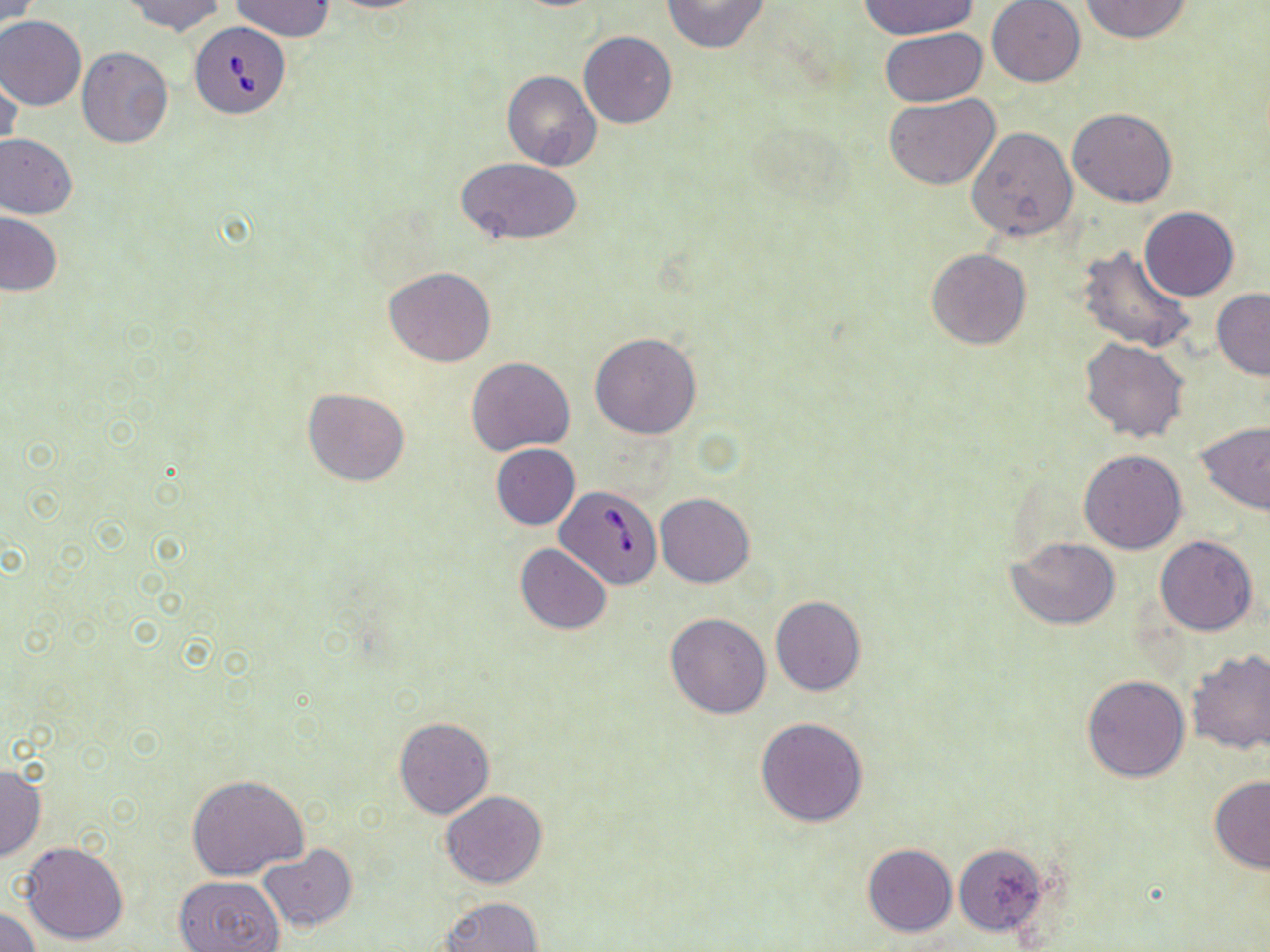 Approximate bounding boxes as [x1, y1, x2, y2] in pixels. Babesia divergens-infected red blood cell locations: [191, 22, 290, 119], [556, 486, 657, 586]. Uninfected red blood cell locations: [119, 0, 228, 36], [231, 0, 333, 40], [321, 0, 435, 12], [662, 0, 771, 52], [858, 0, 980, 39], [1081, 0, 1192, 44], [2, 1, 41, 27], [986, 1, 1085, 87], [0, 16, 87, 110], [880, 28, 987, 106], [579, 31, 677, 129], [77, 48, 174, 150], [1, 68, 22, 161], [501, 70, 601, 172], [884, 92, 1000, 190], [1067, 106, 1177, 207], [965, 127, 1078, 242], [0, 133, 78, 220], [458, 158, 583, 247], [1138, 206, 1240, 301], [1, 212, 62, 298], [1077, 245, 1196, 354], [926, 248, 1032, 349], [384, 267, 496, 367], [1212, 289, 1270, 380], [590, 332, 702, 439], [1080, 337, 1190, 444], [467, 356, 574, 455], [304, 387, 411, 486], [1195, 420, 1270, 514], [490, 444, 581, 530], [1078, 449, 1187, 553], [656, 492, 754, 588], [1156, 535, 1258, 635], [1007, 536, 1120, 629], [515, 543, 612, 635], [770, 597, 867, 696], [665, 612, 772, 718], [1186, 651, 1270, 756], [1082, 674, 1190, 782], [394, 715, 494, 819], [756, 716, 869, 826], [0, 763, 46, 863], [185, 775, 309, 881], [1209, 776, 1270, 872], [441, 790, 548, 889], [19, 841, 129, 946], [862, 843, 956, 936], [258, 844, 356, 931], [954, 844, 1049, 935], [174, 875, 285, 951], [440, 896, 542, 952], [0, 907, 41, 951]. Slide-level diagnosis: Babesia divergens. Optical microscopy. 1000x magnification. May-Grünwald-Giemsa-stained preparation. One field of a larger specimen. Image is 1270×952 pixels. Thin blood film.